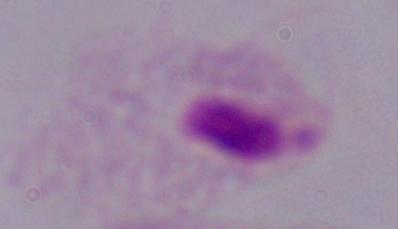

Summary:
  - Modality: photomicrograph
  - Magnification: 1000x
  - Identification: trichomonad